Classify this cell by malaria status.
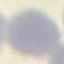

Uninfected.

Summary:
  - Image type: automatically extracted cell patch, resized to 64 × 64 pixels
  - Preparation: thin blood smear
  - Stain: Giemsa
  - Capture: smartphone camera at the microscope eyepiece